Comment on the morphology of the red blood cells.
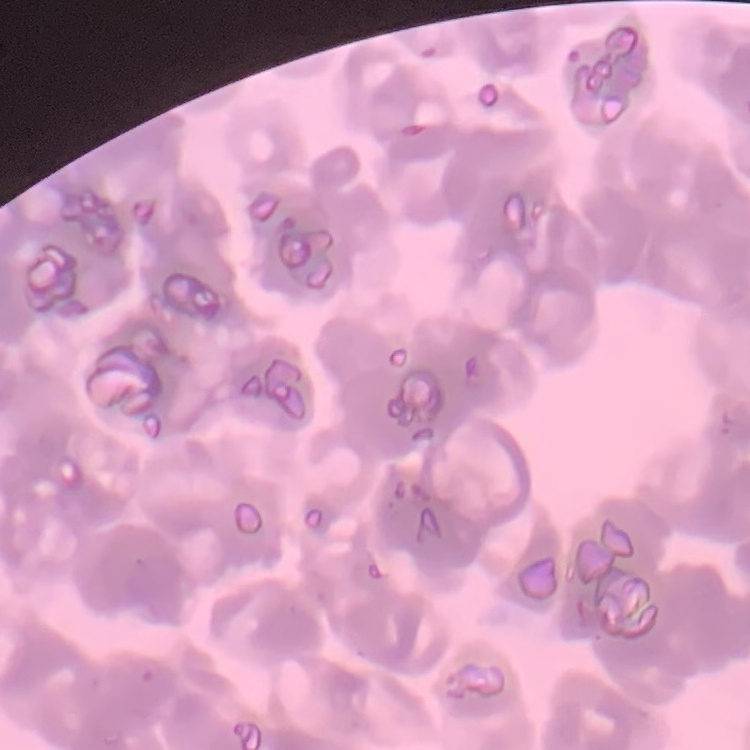

Rouleaux formation.

Field's or Giemsa stain. Thin peripheral smear. One tile cut from a larger photomicrograph.